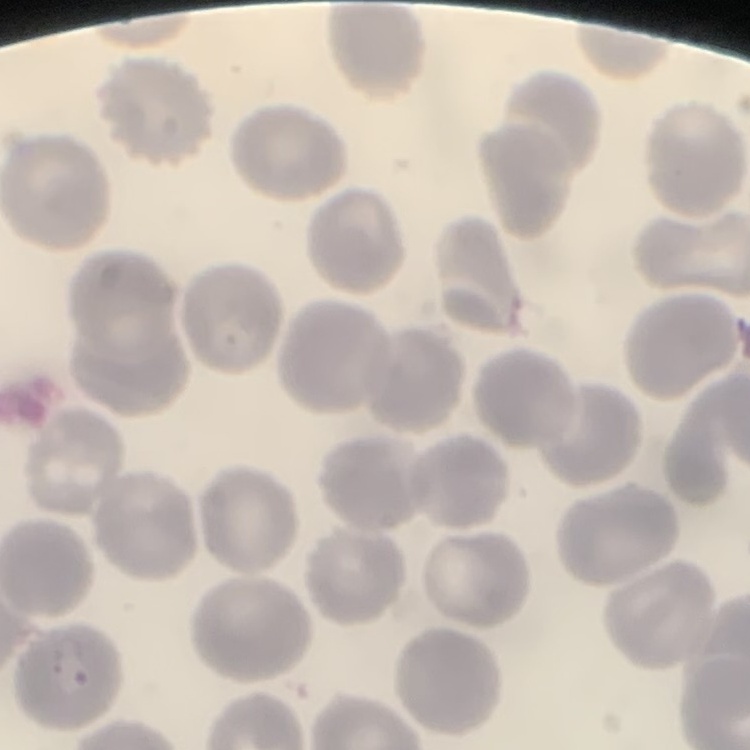
red_blood_cell_morphology: no rouleaux formation
image_type: one tile cut from a larger photomicrograph
preparation: thin blood smear
stain: Field's or Giemsa